Assess this cell for malaria.
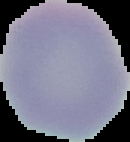
It is uninfected.

preparation = thin blood film
image type = segmented cell region with the area outside set to black
image size = 130×142 pixels